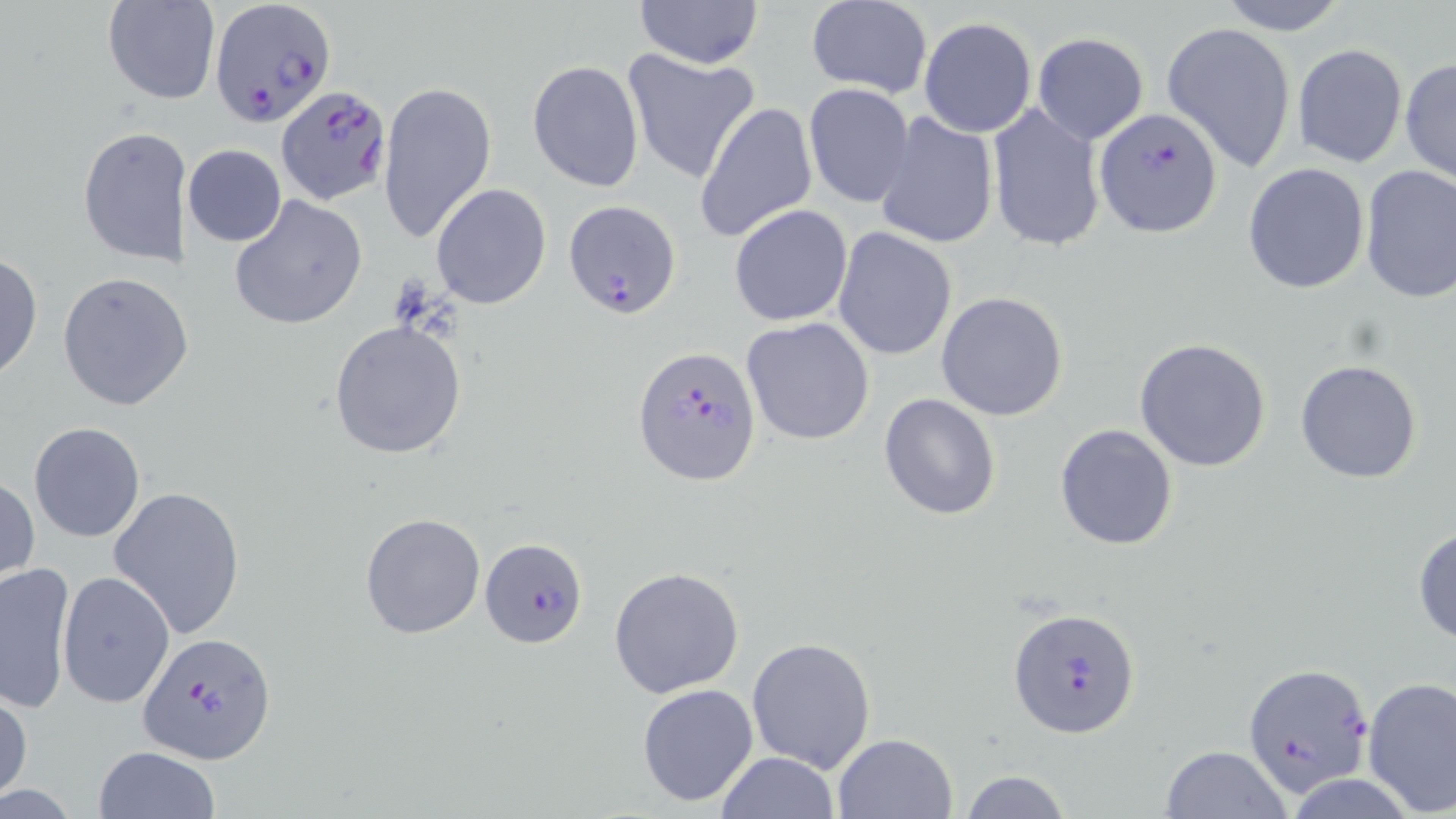 Approximate bounding boxes as [x1, y1, x2, y2] in pixels. Uninfected red blood cell locations: [635, 0, 764, 70], [1214, 0, 1351, 36], [102, 1, 220, 106], [805, 1, 931, 97], [918, 17, 1037, 138], [1162, 21, 1297, 173], [1032, 32, 1149, 145], [1292, 42, 1408, 170], [623, 47, 758, 185], [1400, 56, 1456, 187], [528, 60, 643, 192], [377, 78, 496, 248], [804, 82, 914, 208], [695, 101, 818, 243], [988, 103, 1106, 255], [874, 111, 1000, 251], [77, 125, 183, 266], [183, 144, 287, 247], [1242, 162, 1370, 295], [1359, 167, 1455, 304], [431, 183, 552, 311], [228, 194, 369, 330], [729, 203, 853, 326], [833, 227, 958, 361], [0, 250, 42, 385], [57, 270, 191, 411], [935, 292, 1069, 421], [741, 316, 875, 446], [328, 318, 468, 461], [1133, 337, 1273, 472], [1295, 358, 1424, 484], [878, 392, 1002, 521], [29, 422, 145, 542], [1054, 423, 1178, 551], [0, 475, 39, 587], [109, 484, 246, 640], [359, 512, 486, 639], [1413, 523, 1456, 647], [1, 560, 75, 714], [609, 566, 745, 697], [57, 571, 175, 709], [746, 637, 877, 773], [1361, 677, 1456, 816], [636, 683, 759, 808], [0, 687, 32, 805], [832, 732, 957, 818], [1157, 745, 1293, 819], [93, 747, 221, 819], [715, 752, 841, 819], [959, 768, 1072, 819]. Plasmodium falciparum-infected red blood cell locations: [212, 0, 332, 129], [277, 84, 391, 204], [1094, 108, 1223, 239], [563, 199, 684, 320], [634, 346, 762, 488], [480, 538, 587, 649], [1012, 608, 1142, 738], [139, 631, 275, 764], [1241, 661, 1372, 797]. Slide-level diagnosis: Plasmodium falciparum. One field of a larger specimen. Captured at 1000x magnification. Thin blood smear. Optical microscopy. May-Grünwald-Giemsa stain. Image is 1456×819 pixels.